Identify the blood parasite species.
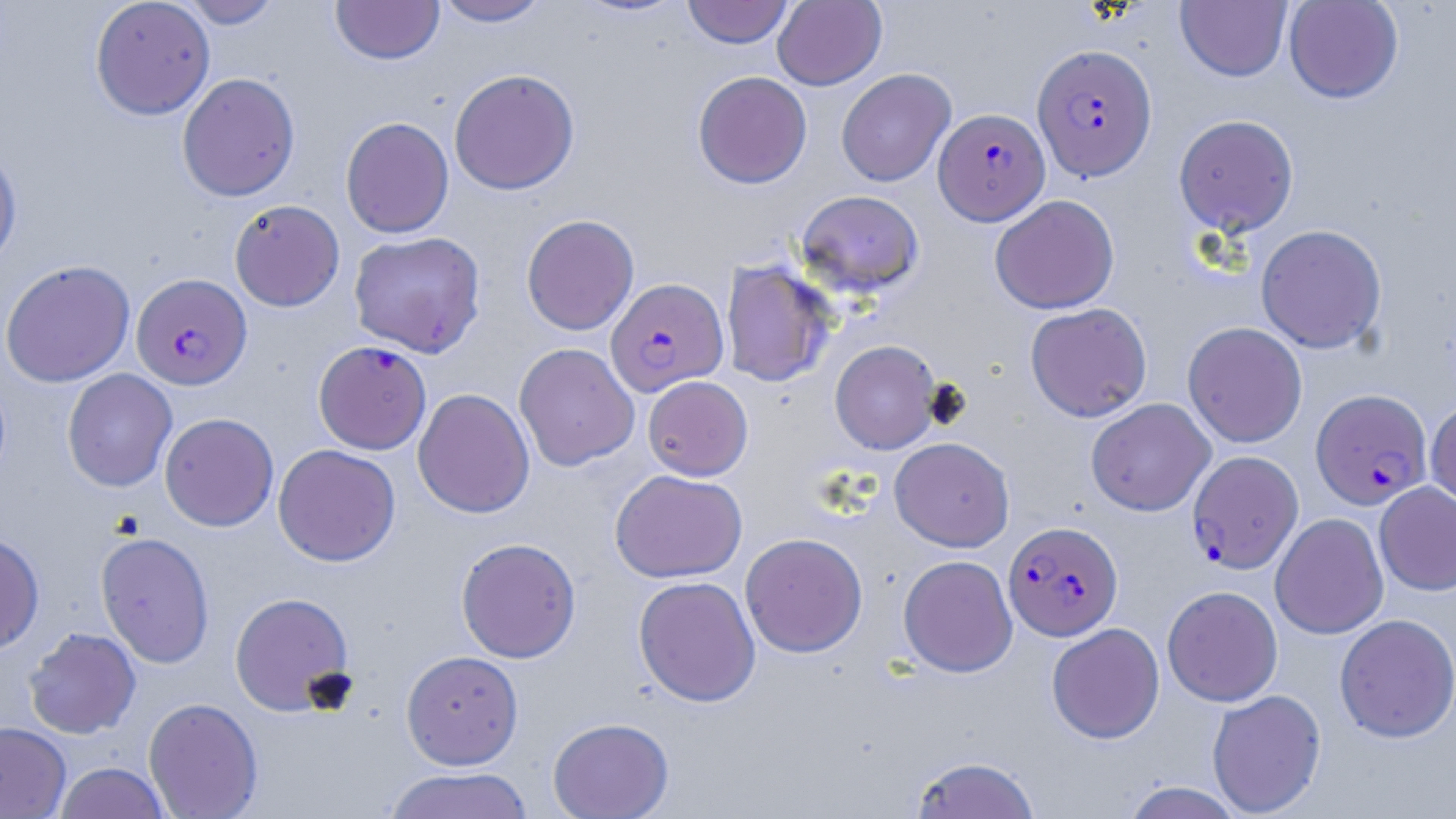
Plasmodium falciparum.

Approximate bounding boxes as (x1, y1, x2, y2) in pixels. Plasmodium falciparum-infected red blood cell locations: (1032, 44, 1157, 181), (934, 108, 1050, 225), (131, 273, 251, 390), (606, 277, 728, 396), (313, 340, 431, 454), (1311, 388, 1432, 509), (1187, 450, 1303, 574), (1004, 521, 1123, 640). Uninfected red blood cell locations: (90, 0, 215, 119), (176, 0, 284, 29), (433, 0, 551, 27), (682, 0, 794, 48), (772, 0, 887, 90), (1284, 0, 1404, 104), (331, 1, 444, 64), (1176, 1, 1292, 82), (836, 68, 955, 187), (449, 69, 580, 195), (693, 71, 812, 188), (177, 72, 300, 201), (1174, 114, 1299, 236), (340, 117, 454, 238), (0, 142, 22, 271), (795, 189, 925, 298), (990, 194, 1119, 314), (229, 199, 345, 311), (521, 214, 639, 335), (1256, 224, 1387, 353), (348, 231, 485, 357), (0, 260, 136, 387), (720, 260, 836, 387), (1025, 302, 1152, 422), (1182, 322, 1307, 448), (830, 340, 942, 454), (514, 343, 639, 471), (62, 368, 177, 492), (642, 375, 753, 480), (413, 388, 535, 518), (1085, 398, 1215, 516), (1426, 398, 1456, 512), (159, 412, 279, 531), (889, 437, 1014, 552), (273, 444, 400, 566), (610, 469, 747, 582), (1374, 482, 1456, 596), (1270, 513, 1389, 639), (95, 532, 214, 668), (0, 533, 45, 654), (740, 533, 867, 657), (456, 537, 581, 663), (898, 554, 1017, 677), (633, 575, 760, 707), (1162, 585, 1283, 707), (229, 592, 355, 716), (1334, 613, 1456, 743), (1046, 623, 1165, 743), (24, 627, 141, 738), (401, 650, 524, 769), (1207, 689, 1327, 817), (143, 697, 263, 818), (547, 717, 674, 819), (0, 722, 71, 818), (907, 755, 1042, 819), (54, 762, 171, 819), (381, 767, 535, 818), (1121, 781, 1246, 819). May-Grünwald-Giemsa-stained preparation. 1000x magnification. Optical microscopy. Image is 1456×819 pixels. Single field of view. Thin blood smear.